Assess the morphology of the erythrocytes.
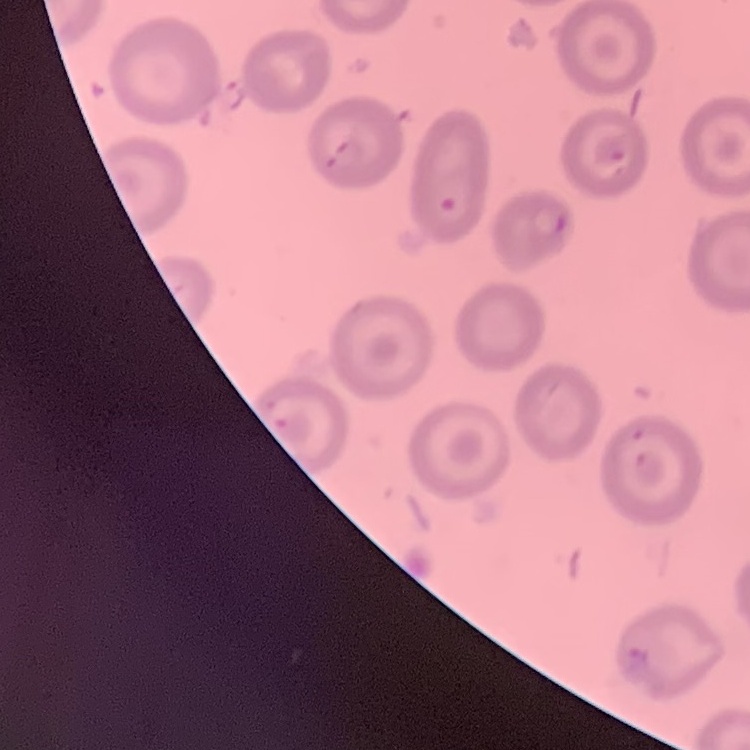
They show no rouleaux formation.

stain = Field's or Giemsa
image type = square crop of a larger photomicrograph
preparation = thin blood smear